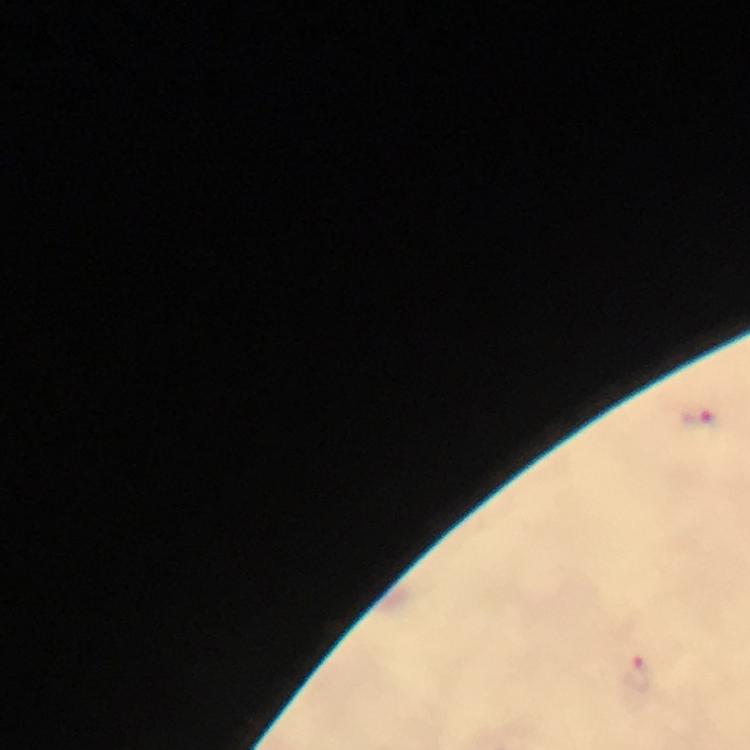
Approximate centers as {x, y} in pixels. Plasmodium parasite locations: {699, 418}, {636, 674}. At 100x magnification. Smartphone photograph taken through a microscope. Thick blood smear. Giemsa stain. Immersion oil applied. Cropped region of a single field of view. Image is 750×750 pixels. From a diagnostic examination for malaria.